Assess the morphology of the red blood cells.
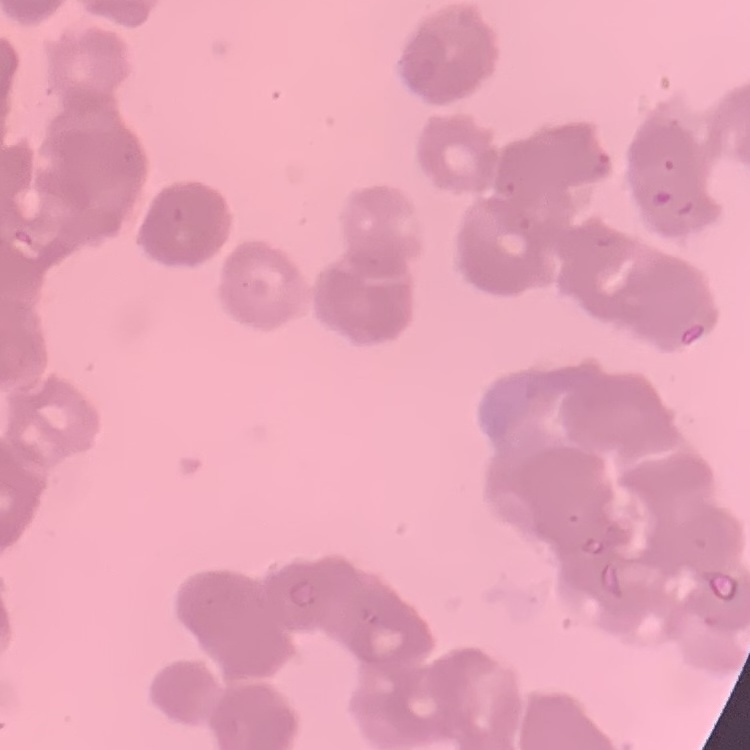
Rouleaux formation.

Summary:
  - Preparation: thin blood film
  - Image type: one tile cut from a larger photomicrograph
  - Stain: Field's or Giemsa